Locate and identify every blood parasite.
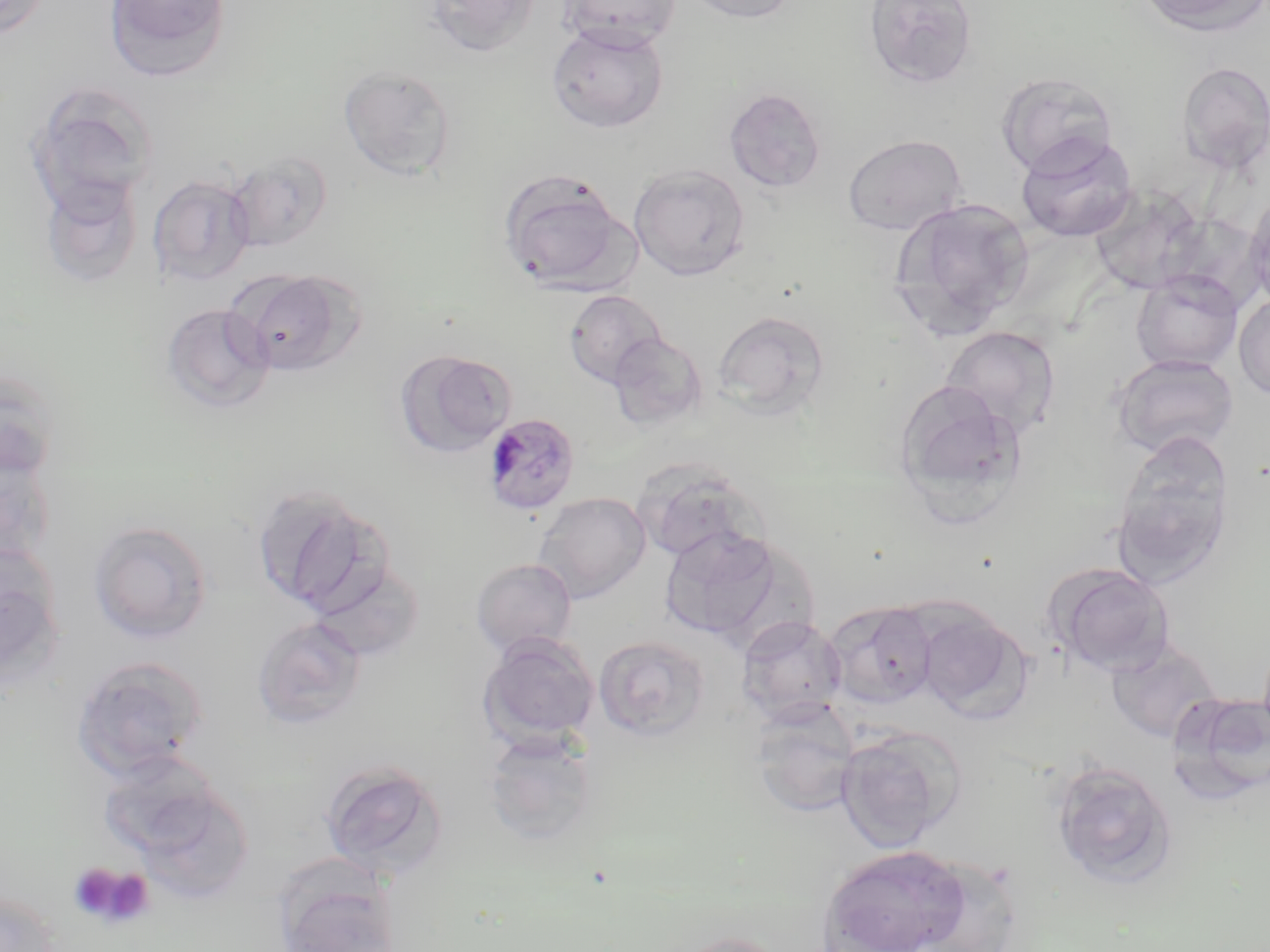

Approximate bounding boxes as named x1/y1/x2/y2 corners in pixels.
Plasmodium malariae-infected red blood cells: (x1=483, y1=412, x2=581, y2=516).
No Plasmodium falciparum, Plasmodium ovale, Plasmodium vivax, Babesia divergens, or Trypanosoma brucei observed.

Summary:
  - Platelet locations: (x1=70, y1=862, x2=154, y2=930)
  - Uninfected red blood cell locations: (x1=0, y1=0, x2=50, y2=39), (x1=102, y1=0, x2=232, y2=83), (x1=422, y1=0, x2=541, y2=58), (x1=559, y1=0, x2=682, y2=50), (x1=683, y1=0, x2=800, y2=23), (x1=864, y1=0, x2=978, y2=88), (x1=1133, y1=0, x2=1269, y2=36), (x1=546, y1=22, x2=670, y2=134), (x1=1176, y1=61, x2=1270, y2=175), (x1=338, y1=65, x2=457, y2=181), (x1=997, y1=73, x2=1116, y2=175), (x1=25, y1=82, x2=160, y2=212), (x1=725, y1=87, x2=826, y2=194), (x1=1015, y1=131, x2=1138, y2=243), (x1=842, y1=133, x2=968, y2=236), (x1=225, y1=150, x2=333, y2=252), (x1=629, y1=162, x2=751, y2=280), (x1=498, y1=167, x2=636, y2=295), (x1=148, y1=173, x2=256, y2=287), (x1=38, y1=174, x2=144, y2=288), (x1=1087, y1=184, x2=1207, y2=294), (x1=1244, y1=193, x2=1270, y2=309), (x1=888, y1=197, x2=1035, y2=338), (x1=235, y1=270, x2=362, y2=377), (x1=1131, y1=271, x2=1244, y2=373), (x1=564, y1=289, x2=666, y2=387), (x1=1234, y1=293, x2=1270, y2=401), (x1=160, y1=302, x2=275, y2=414), (x1=712, y1=310, x2=830, y2=417), (x1=940, y1=326, x2=1061, y2=442), (x1=608, y1=333, x2=708, y2=431), (x1=395, y1=349, x2=516, y2=458), (x1=1113, y1=354, x2=1239, y2=459), (x1=0, y1=367, x2=62, y2=481), (x1=893, y1=381, x2=1027, y2=521), (x1=1112, y1=438, x2=1234, y2=589), (x1=0, y1=445, x2=57, y2=566), (x1=635, y1=463, x2=762, y2=565), (x1=251, y1=483, x2=388, y2=614), (x1=533, y1=491, x2=651, y2=603), (x1=89, y1=520, x2=214, y2=642), (x1=658, y1=526, x2=785, y2=642), (x1=0, y1=544, x2=66, y2=688), (x1=309, y1=558, x2=424, y2=662), (x1=471, y1=558, x2=577, y2=656), (x1=1048, y1=564, x2=1176, y2=677), (x1=823, y1=601, x2=938, y2=709), (x1=916, y1=606, x2=1029, y2=720), (x1=253, y1=615, x2=367, y2=730), (x1=737, y1=615, x2=847, y2=724), (x1=478, y1=632, x2=600, y2=749), (x1=593, y1=634, x2=711, y2=741), (x1=1105, y1=639, x2=1220, y2=743), (x1=70, y1=655, x2=210, y2=780), (x1=1167, y1=691, x2=1270, y2=805), (x1=749, y1=700, x2=861, y2=817), (x1=835, y1=726, x2=966, y2=852), (x1=481, y1=728, x2=600, y2=846), (x1=97, y1=752, x2=246, y2=874), (x1=319, y1=759, x2=450, y2=880), (x1=1051, y1=760, x2=1177, y2=889), (x1=818, y1=844, x2=973, y2=952), (x1=908, y1=859, x2=1025, y2=952), (x1=276, y1=876, x2=401, y2=952), (x1=0, y1=889, x2=62, y2=952), (x1=668, y1=930, x2=792, y2=952)
  - Slide-level diagnosis: Plasmodium malariae
  - Field of view: one of a larger specimen
  - Stain: May-Grünwald-Giemsa
  - Image size: 1270×952 pixels
  - Preparation: thin blood film
  - Magnification: 1000x
  - Modality: optical microscopy